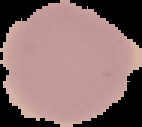
Result: negative for malaria parasites. Segmented cell region on a black background. From a thin blood film. Image is 142×127 pixels.